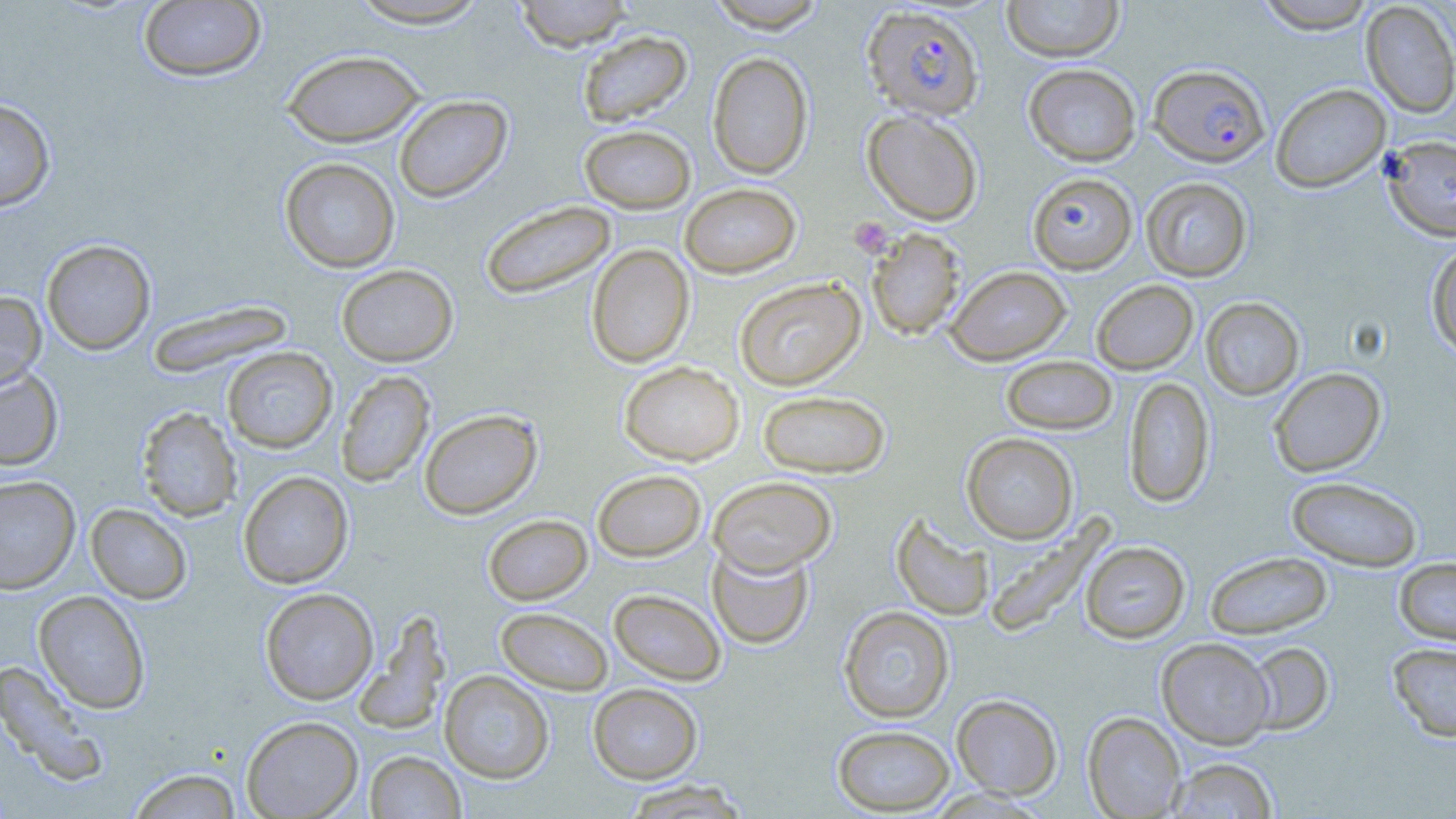
Summary:
  - Coordinate format: approximate bounding boxes as (x1, y1, x2, y2) in pixels
  - Uninfected red blood cell locations: (345, 0, 494, 29), (511, 0, 635, 51), (705, 0, 827, 33), (1002, 0, 1124, 62), (1254, 0, 1377, 33), (138, 1, 266, 82), (1360, 2, 1456, 119), (577, 30, 692, 127), (282, 49, 425, 147), (707, 51, 814, 179), (1023, 63, 1142, 166), (1271, 83, 1391, 193), (394, 94, 513, 203), (0, 98, 55, 212), (862, 109, 984, 226), (579, 124, 696, 214), (1381, 135, 1456, 241), (279, 157, 400, 273), (1027, 172, 1137, 274), (1140, 177, 1252, 282), (679, 182, 802, 279), (480, 200, 617, 300), (866, 228, 966, 341), (41, 239, 156, 355), (1426, 242, 1456, 358), (586, 244, 695, 368), (336, 264, 458, 367), (946, 265, 1072, 365), (734, 277, 866, 391), (1091, 280, 1198, 375), (0, 291, 46, 392), (1200, 297, 1305, 400), (147, 300, 295, 378), (222, 347, 338, 453), (1000, 355, 1118, 436), (619, 360, 744, 466), (0, 367, 64, 471), (1269, 368, 1386, 477), (335, 370, 435, 488), (1123, 376, 1215, 509), (757, 390, 892, 478), (136, 407, 242, 522), (419, 408, 542, 519), (961, 433, 1079, 544), (592, 469, 707, 562), (238, 470, 354, 589), (0, 475, 80, 594), (1286, 475, 1423, 571), (708, 476, 837, 576), (85, 503, 193, 604), (891, 512, 995, 622), (483, 514, 593, 605), (983, 517, 1114, 638), (1080, 541, 1191, 643), (707, 543, 814, 650), (1204, 551, 1333, 639), (1394, 557, 1456, 647), (260, 588, 379, 705), (608, 588, 727, 686), (34, 590, 151, 714), (838, 606, 955, 723), (496, 607, 613, 694), (353, 610, 452, 736), (1156, 637, 1275, 749), (1244, 641, 1335, 736), (1388, 642, 1456, 742), (0, 660, 110, 786), (439, 670, 554, 783), (588, 683, 703, 783), (951, 694, 1063, 799), (1083, 712, 1186, 818), (241, 715, 363, 818), (832, 724, 956, 815), (365, 751, 466, 818), (1164, 757, 1280, 818), (126, 767, 244, 818), (618, 780, 754, 818)
  - Plasmodium falciparum-infected red blood cell locations: (862, 4, 985, 122), (1148, 63, 1270, 168)
  - Platelet locations: (849, 217, 893, 257)
  - Slide-level diagnosis: Plasmodium falciparum
  - Modality: light microscopy
  - Field of view: single
  - Preparation: thin blood film
  - Stain: May-Grünwald-Giemsa
  - Magnification: 1000x
  - Image size: 1456×819 pixels